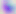

Summary:
  - Magnification: 400x
  - Modality: photomicrograph
  - Identification: Toxoplasma gondii